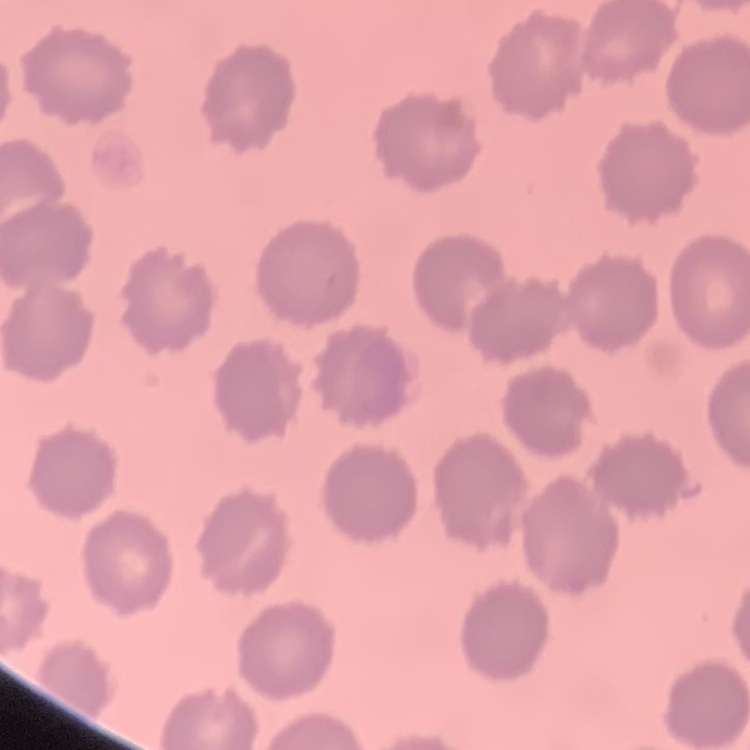

Summary:
  - Erythrocyte morphology: no rouleaux formation
  - Preparation: thin peripheral smear
  - Image type: one tile cut from a larger photomicrograph
  - Stain: Field's or Giemsa